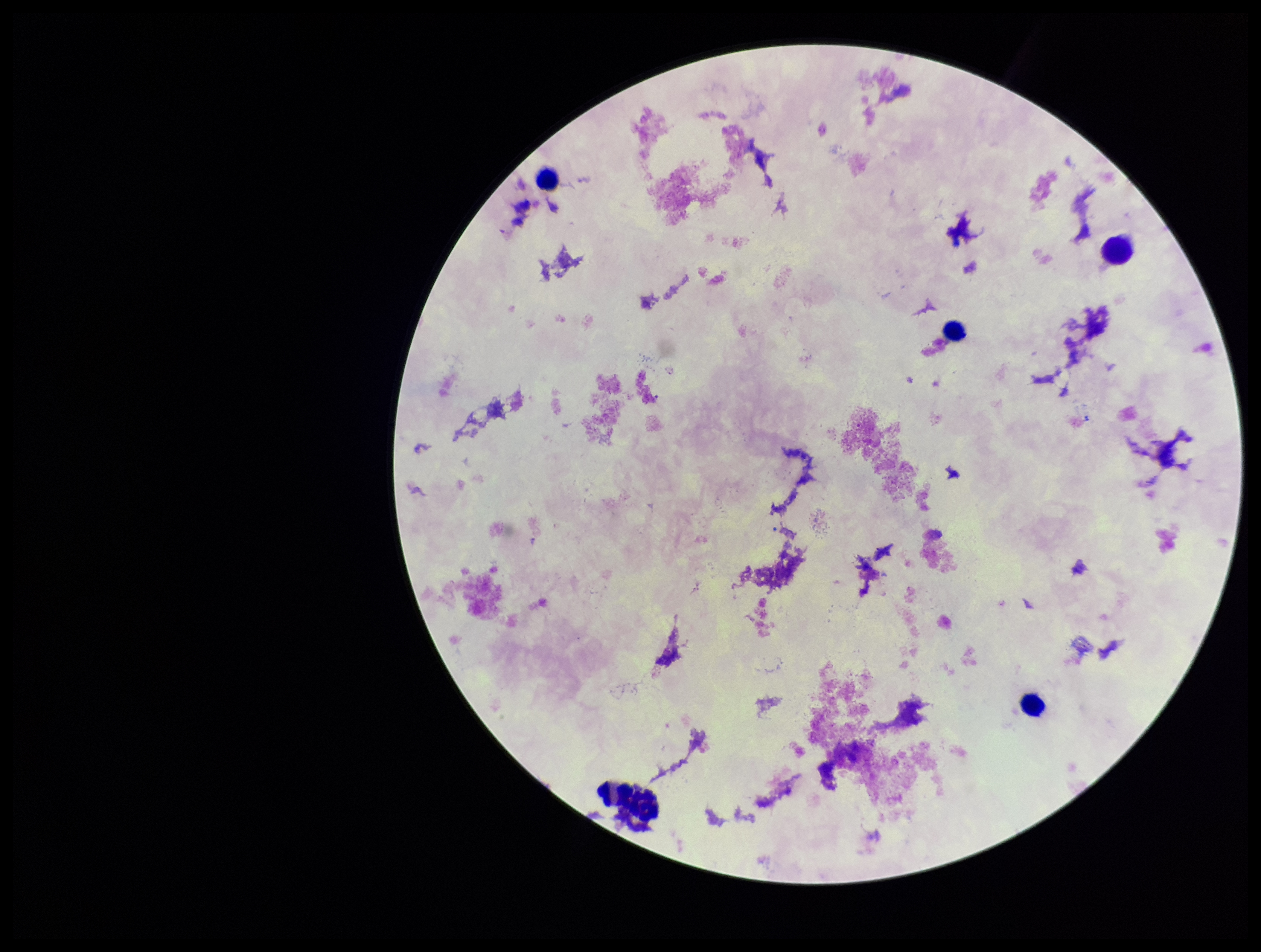
patient malaria status = negative
capture = smartphone photograph through the microscope eyepiece
field of view = single
Plasmodium parasites = none detected
preparation = thick
parasite count = 0
stain = Giemsa
leukocyte count = 5
image size = 1261×952 pixels